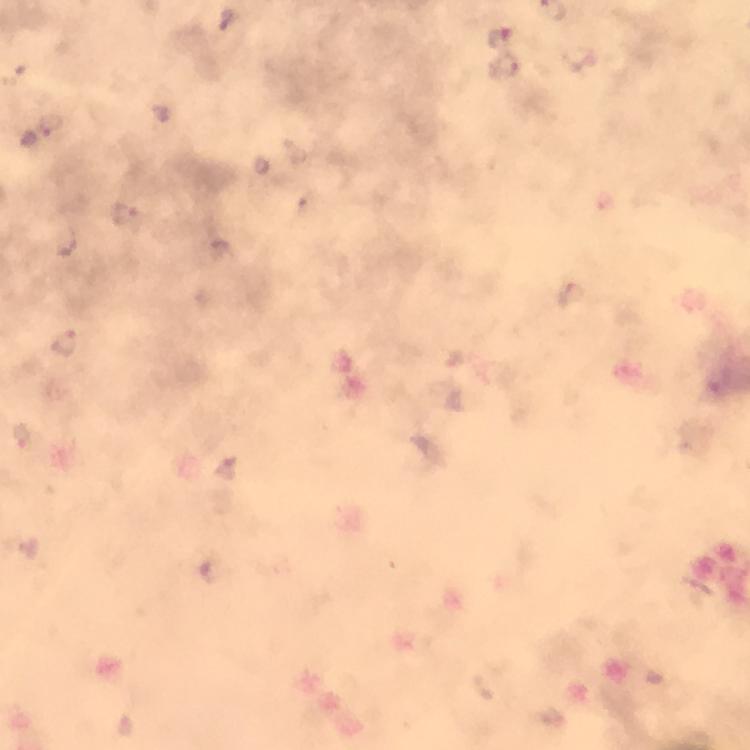
Approximate centers as {x, y} in pixels.
Summary:
  - Malaria parasite locations: {499, 37}, {504, 66}, {51, 124}, {126, 215}, {67, 342}, {226, 469}
  - Image size: 750×750 pixels
  - Immersion oil: used
  - Stain: Giemsa
  - Magnification: 100x
  - Preparation: thick blood smear
  - Cropped from: a single field of view
  - Context: from a malaria diagnostic workup
  - Capture: smartphone camera through the microscope